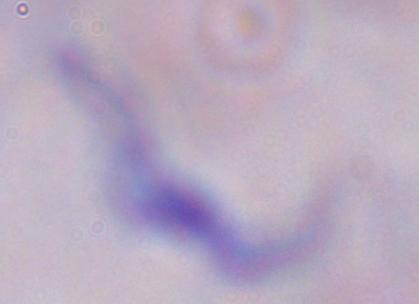
magnification = 1000x
modality = micrograph
identification = trypanosome